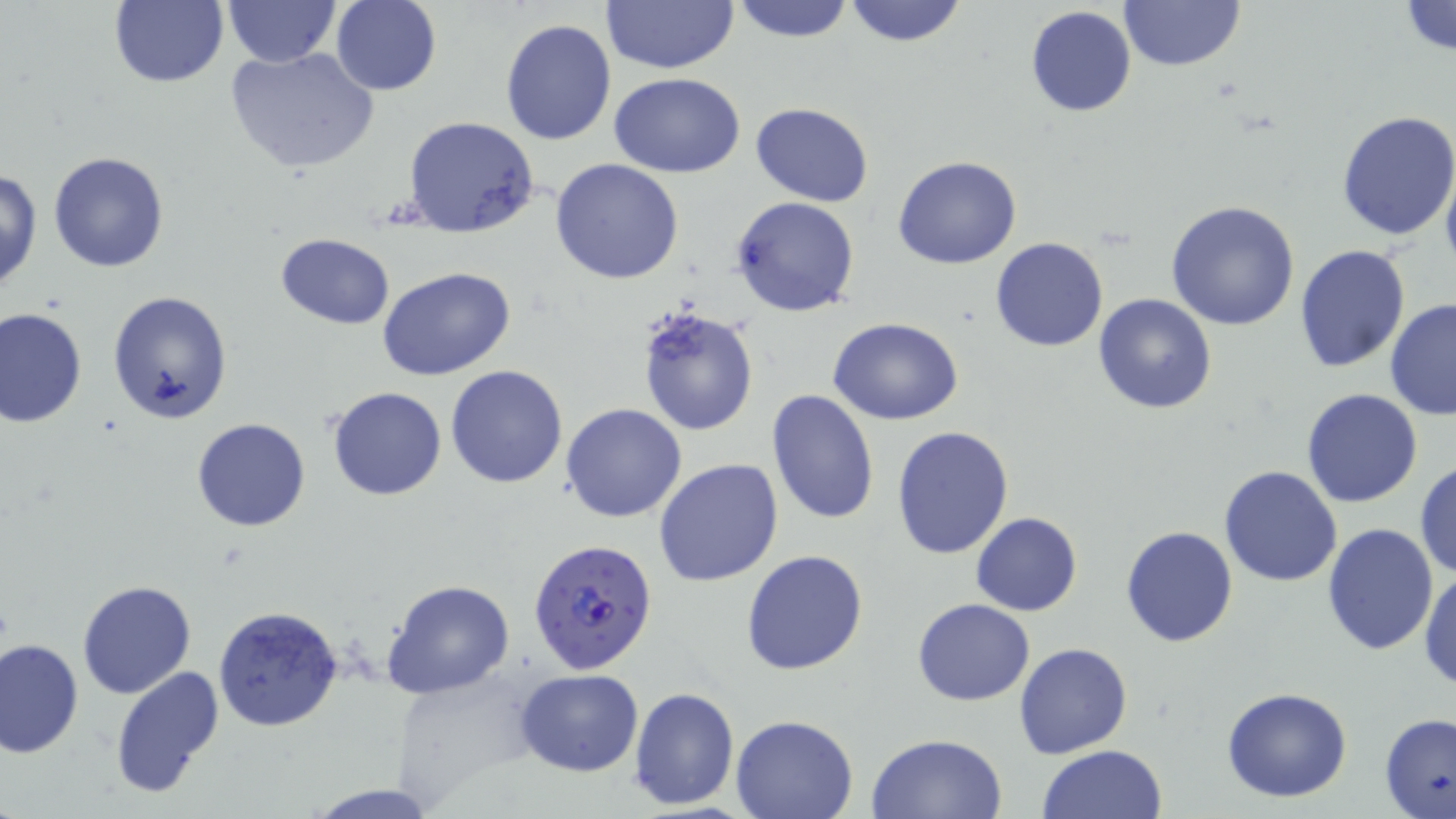 Approximate bounding boxes as [x1, y1, x2, y2] in pixels. Plasmodium falciparum-infected red blood cell locations: [529, 538, 658, 675]. Uninfected red blood cell locations: [730, 0, 856, 43], [1119, 0, 1244, 70], [109, 1, 228, 88], [222, 1, 340, 67], [600, 1, 738, 75], [842, 1, 969, 48], [1397, 1, 1456, 56], [331, 2, 440, 96], [1024, 6, 1136, 118], [499, 18, 618, 145], [225, 46, 380, 175], [609, 71, 746, 177], [751, 103, 873, 205], [1335, 111, 1456, 242], [403, 117, 541, 238], [47, 151, 168, 273], [894, 156, 1022, 269], [550, 159, 685, 285], [1441, 164, 1456, 272], [1, 169, 44, 292], [730, 196, 860, 318], [1166, 201, 1300, 331], [275, 233, 394, 329], [990, 236, 1108, 352], [1294, 244, 1412, 373], [378, 266, 518, 382], [106, 290, 231, 424], [1092, 293, 1218, 414], [1384, 298, 1456, 419], [636, 304, 761, 434], [1, 307, 86, 427], [829, 316, 963, 425], [445, 364, 568, 487], [327, 386, 446, 501], [766, 388, 882, 526], [1302, 388, 1423, 508], [561, 403, 687, 522], [191, 418, 310, 533], [891, 424, 1014, 560], [654, 459, 784, 587], [1414, 460, 1456, 581], [1220, 465, 1344, 586], [970, 511, 1083, 617], [1320, 521, 1438, 656], [1120, 526, 1238, 646], [740, 550, 868, 676], [1419, 568, 1456, 695], [379, 576, 515, 700], [76, 578, 196, 698], [914, 599, 1035, 705], [213, 605, 343, 731], [0, 637, 83, 757], [1014, 642, 1132, 758], [110, 665, 225, 800], [515, 668, 644, 777], [391, 670, 540, 808], [629, 686, 739, 810], [1222, 686, 1352, 803], [1379, 712, 1456, 819], [729, 715, 858, 819], [865, 733, 1010, 819], [1036, 744, 1167, 819], [305, 782, 441, 817]. Slide-level diagnosis: Plasmodium falciparum. May-Grünwald-Giemsa-stained preparation. Optical microscopy. Image is 1456×819 pixels. Single field of view. Thin blood smear. 1000x magnification.